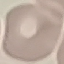

Result: no malaria parasites seen. Photographed with a smartphone camera at the microscope eyepiece. Cell patch, automatically extracted from a larger field of view and resized to 64 × 64 pixels. Thin blood smear. Giemsa stain.